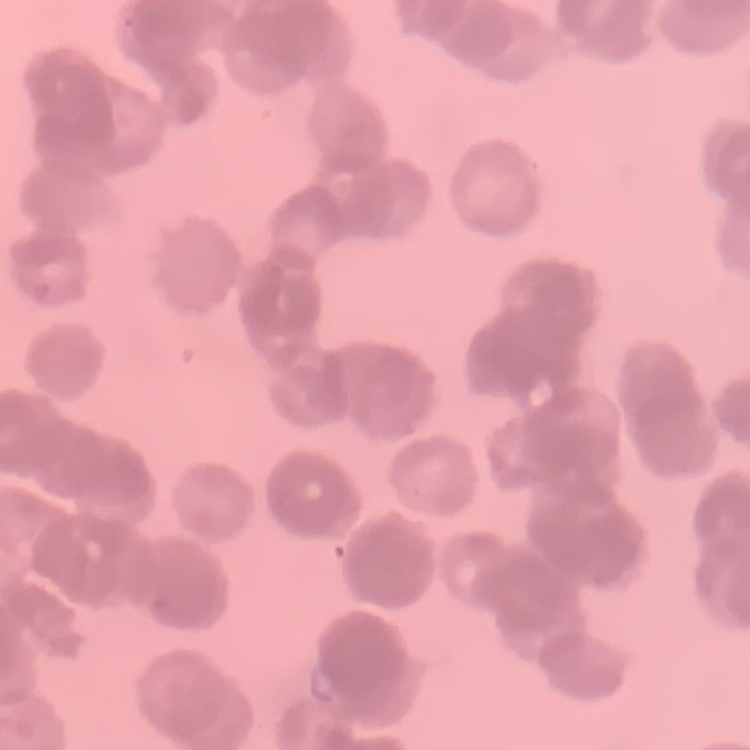

erythrocyte morphology = rouleaux formation
stain = Field's or Giemsa
preparation = thin peripheral smear
image type = one tile cut from a larger photomicrograph